Comment on the morphology of the red blood cells.
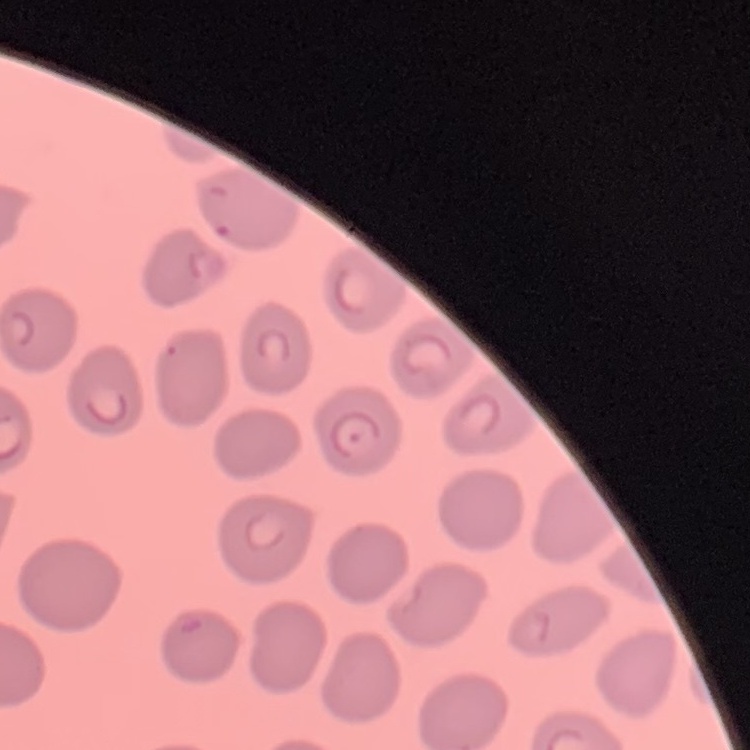

No rouleaux formation.

Summary:
  - Image type: one tile cut from a larger photomicrograph
  - Preparation: thin blood film
  - Stain: Field's or Giemsa